Name the parasite shown.
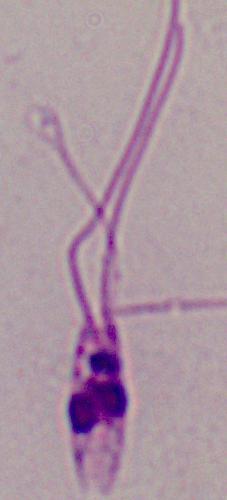
This is Leishmania.

magnification: 1000x
modality: photomicrograph